Locate and identify every blood parasite.
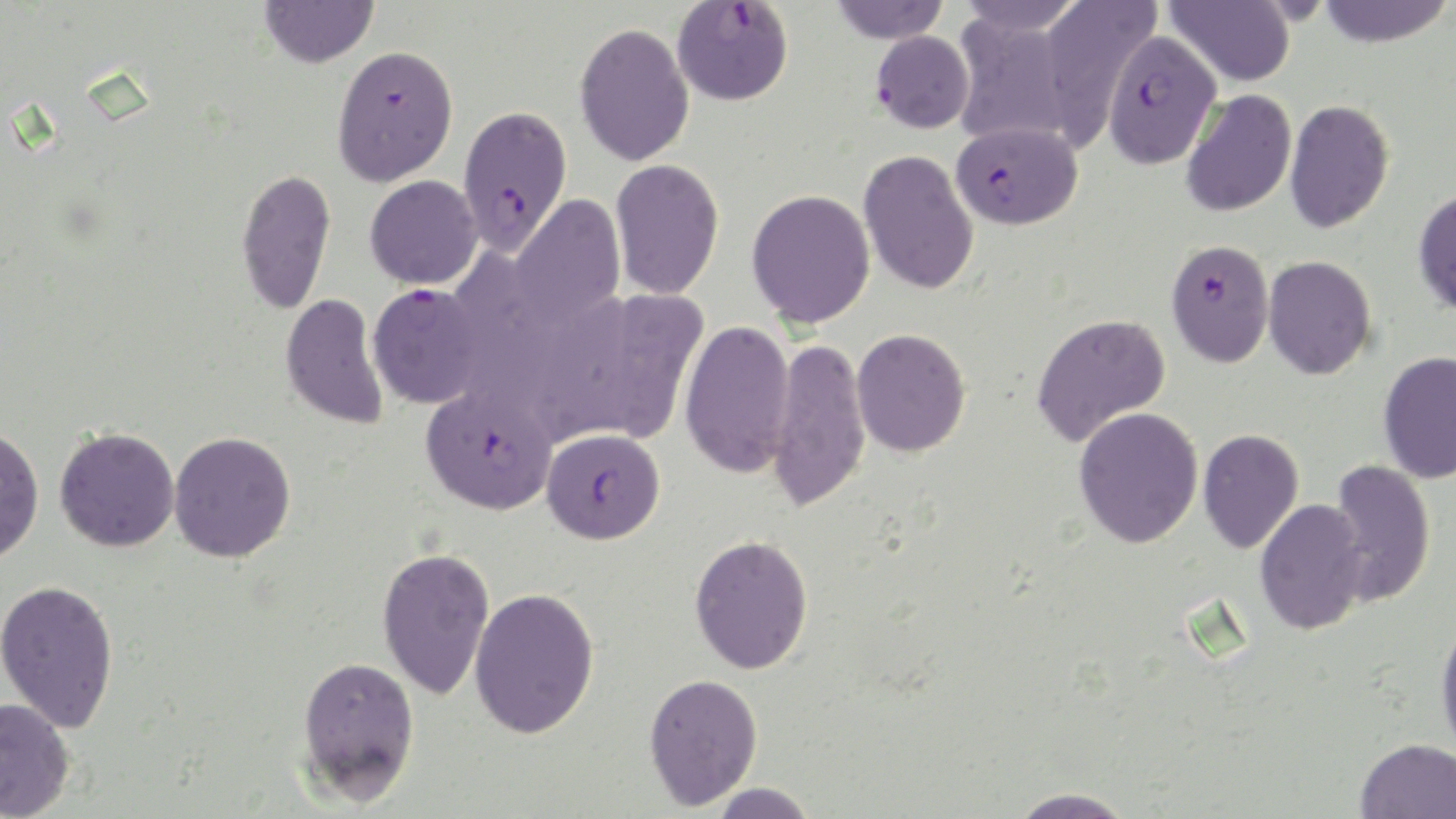
Approximate bounding boxes as [x1, y1, x2, y2] in pixels.
Plasmodium falciparum-infected red blood cells: [671, 1, 794, 105], [871, 30, 974, 133], [1101, 30, 1223, 169], [331, 44, 458, 187], [457, 105, 572, 255], [951, 121, 1082, 230], [1166, 239, 1275, 367], [367, 282, 485, 408], [421, 386, 556, 515], [540, 427, 665, 544].
No Plasmodium ovale, Plasmodium malariae, Plasmodium vivax, Babesia divergens, or Trypanosoma brucei observed.

Uninfected red blood cell locations: [260, 0, 378, 68], [829, 0, 950, 44], [953, 0, 1087, 37], [1036, 0, 1161, 147], [1164, 0, 1297, 87], [1316, 0, 1454, 48], [951, 13, 1079, 147], [574, 22, 695, 167], [1181, 89, 1297, 218], [1284, 98, 1394, 234], [858, 149, 980, 296], [610, 158, 725, 300], [235, 167, 337, 313], [365, 175, 483, 289], [1413, 188, 1456, 316], [746, 189, 876, 328], [510, 195, 625, 328], [1263, 255, 1377, 380], [573, 287, 709, 445], [280, 293, 389, 430], [1030, 312, 1171, 447], [679, 319, 794, 478], [851, 328, 971, 457], [767, 336, 872, 515], [1377, 350, 1456, 482], [1073, 406, 1204, 548], [0, 425, 44, 564], [54, 426, 180, 552], [1198, 428, 1304, 554], [169, 431, 296, 562], [1326, 459, 1437, 606], [1254, 499, 1371, 636], [689, 534, 814, 674], [376, 546, 495, 701], [0, 578, 120, 733], [469, 587, 600, 739], [1435, 614, 1456, 760], [296, 654, 420, 806], [643, 673, 764, 809], [0, 697, 75, 819], [1355, 738, 1456, 819], [707, 782, 818, 819], [1006, 787, 1138, 819]. Slide-level diagnosis: Plasmodium falciparum. Light microscopy. Image is 1456×819 pixels. Thin blood film. 1000x magnification. Single field of view. May-Grünwald-Giemsa-stained preparation.